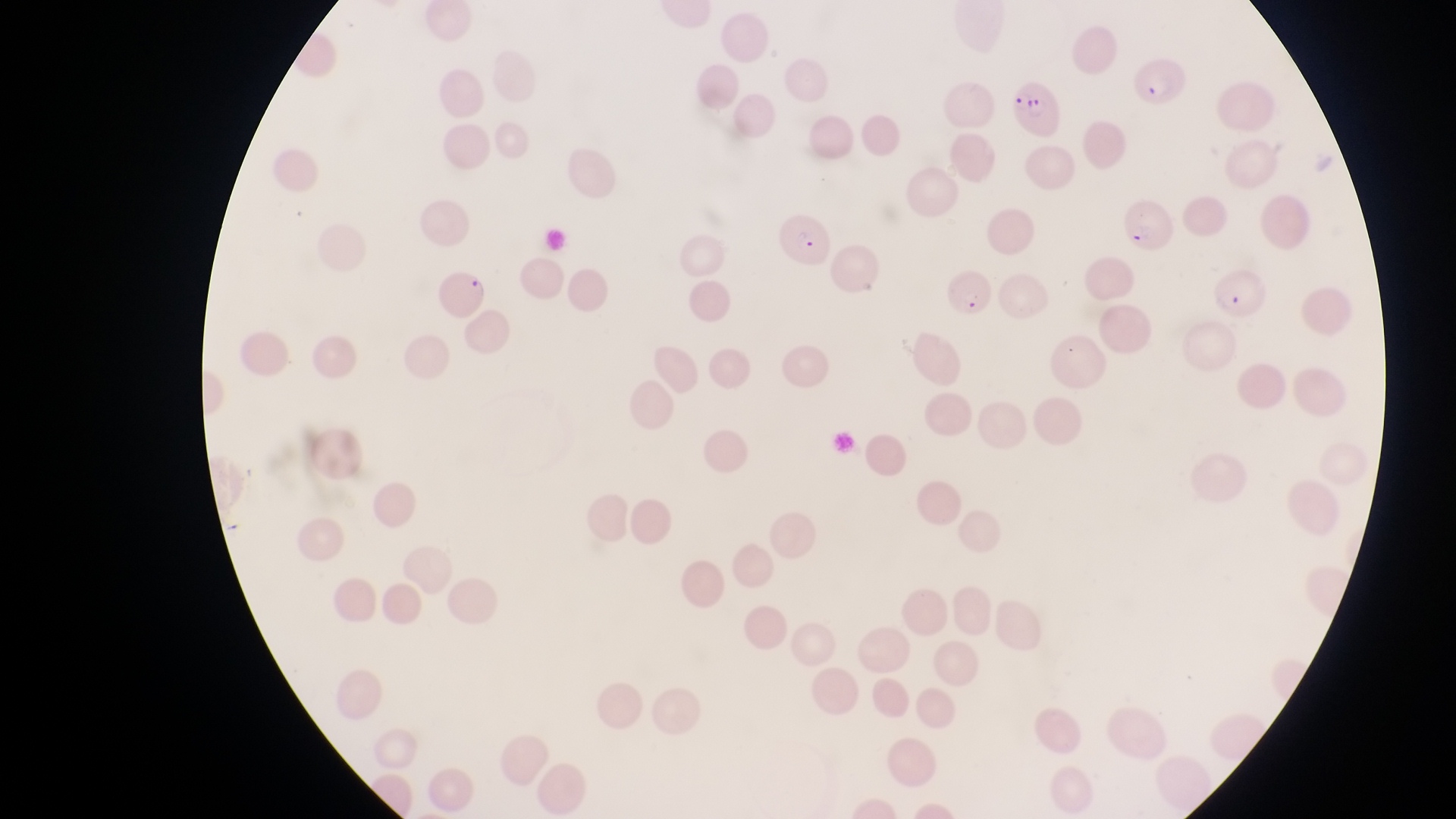
Approximate bounding boxes as left top right bottom in pixels. Parasitised red blood cell locations: 1129 58 1189 114; 1010 80 1068 140; 1122 195 1182 264; 774 215 837 274; 944 258 990 317; 442 267 489 322; 1213 271 1271 327. Single field of view. Sample from Uganda. Thin blood film. Magnification of 1000x. Image is 1456×819 pixels. Photographed through the eyepiece of an Olympus CX-23 microscope with a smartphone camera.